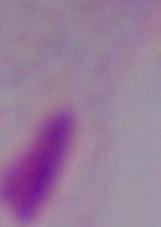

identification = trichomonad
modality = micrograph
magnification = 1000x